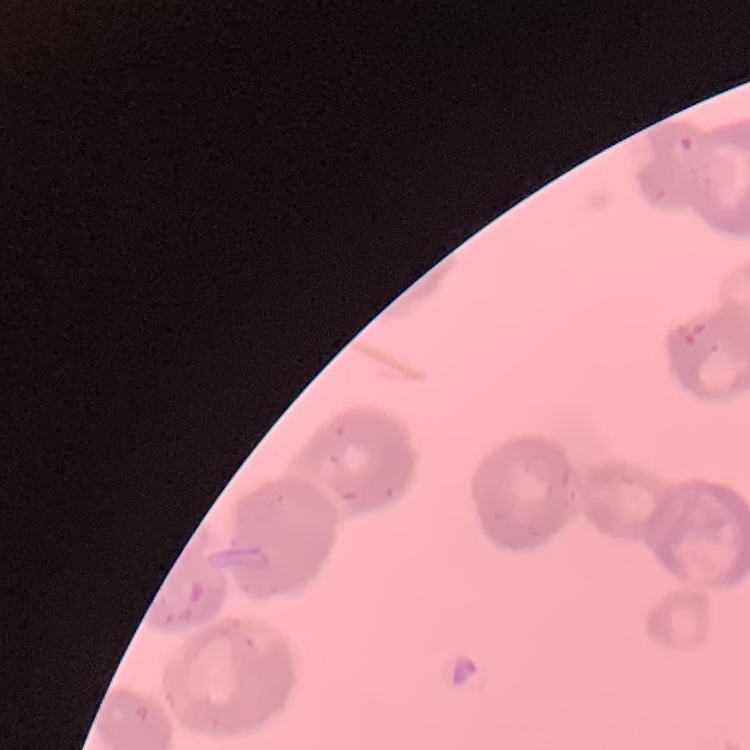
Summary:
  - Red blood cell morphology: rouleaux formation
  - Preparation: thin blood smear
  - Stain: Field's or Giemsa
  - Image type: square crop of a larger photomicrograph